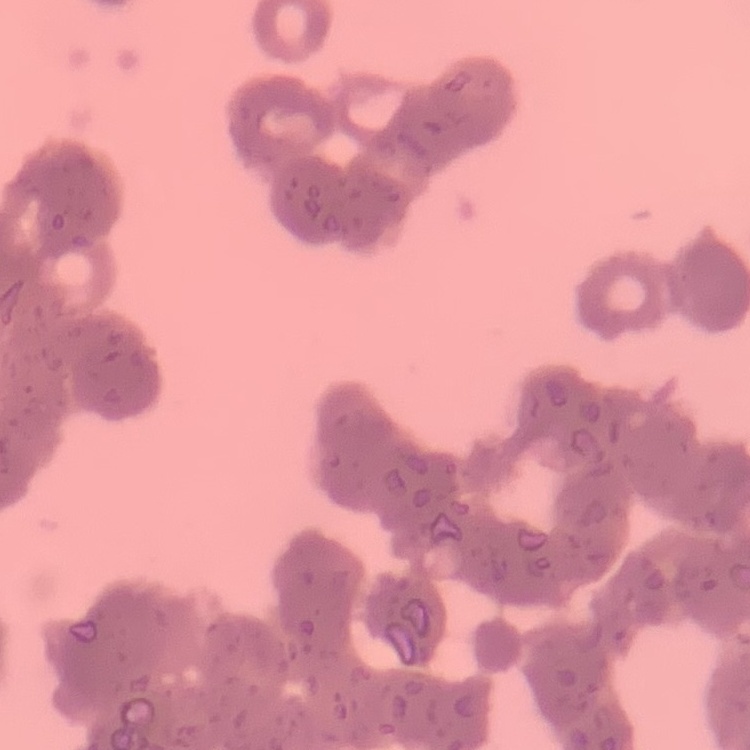
erythrocyte morphology = rouleaux formation
image type = one tile cut from a larger photomicrograph
stain = Field's or Giemsa
preparation = thin blood film